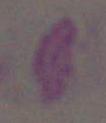 Photomicrograph. Toxoplasma gondii is shown. 1000x magnification.